Classify this cell by malaria status.
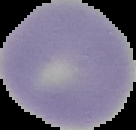
Uninfected.

image size = 136×130 pixels
preparation = thin blood film
image type = cell region segmented out of the field of view; surrounding area masked to black